Locate every Plasmodium parasite.
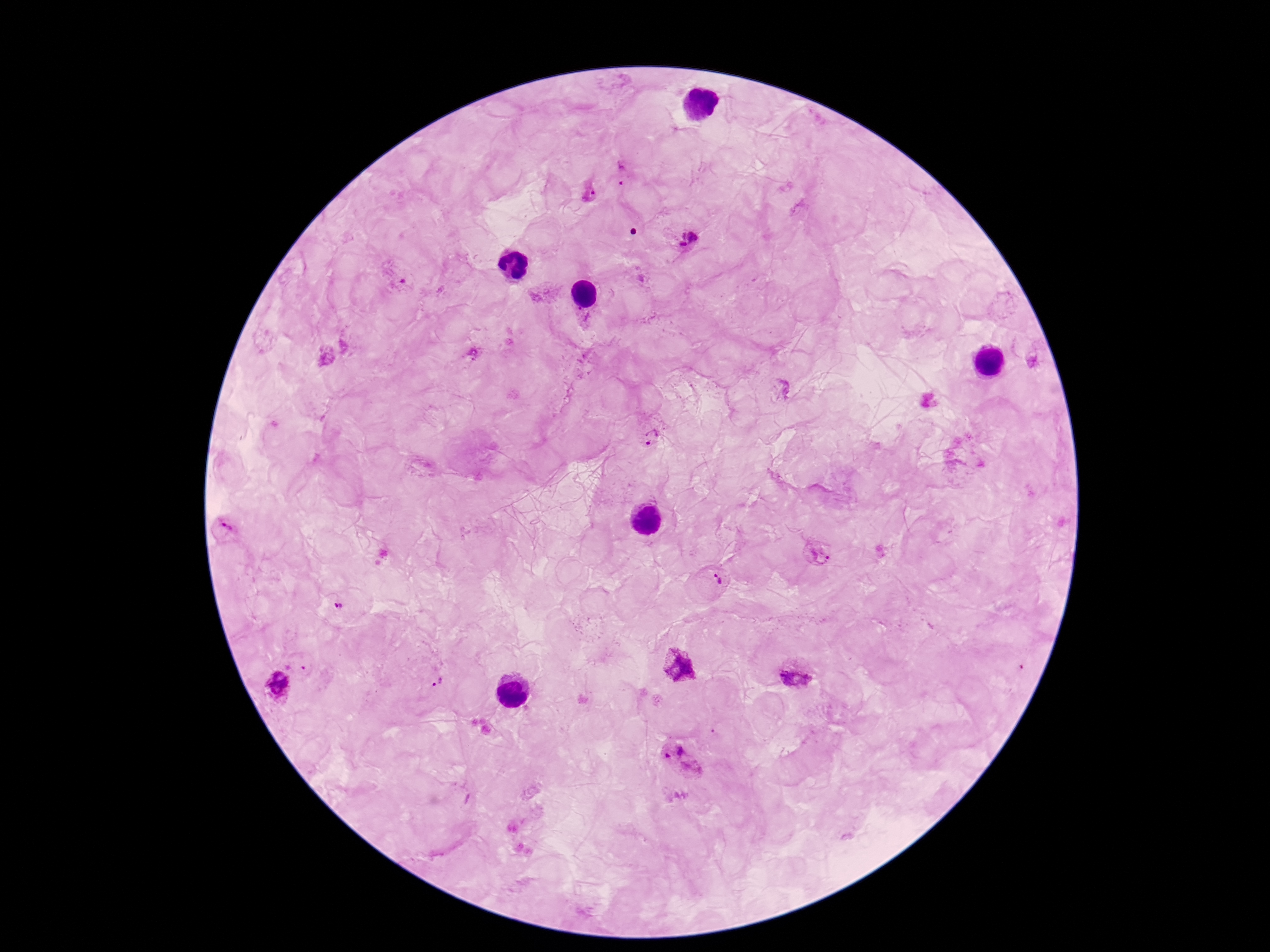
Approximate centers as (x, y) in pixels.
Plasmodium parasites: (622, 172), (590, 190), (687, 237), (653, 436), (225, 529), (817, 554), (714, 581), (340, 609), (677, 666), (796, 672), (438, 682), (279, 684), (684, 761).

Summary:
  - Stain: Giemsa
  - Patient malaria status: positive
  - Magnification: 100x
  - Capture: smartphone camera through the microscope eyepiece
  - Preparation: thick blood film
  - Field of view: single
  - Image size: 1270×952 pixels